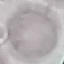

Summary:
  - Result: negative for malaria parasites
  - Image type: cell patch, automatically extracted from a larger field of view and resized to 64 × 64 pixels
  - Stain: Giemsa
  - Preparation: thin blood smear
  - Capture: smartphone through the microscope eyepiece